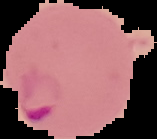
Summary:
  - Image type: cell region segmented out of the field of view; surrounding area masked to black
  - Image size: 157×139 pixels
  - Preparation: thin blood smear
  - Malaria status: parasitized